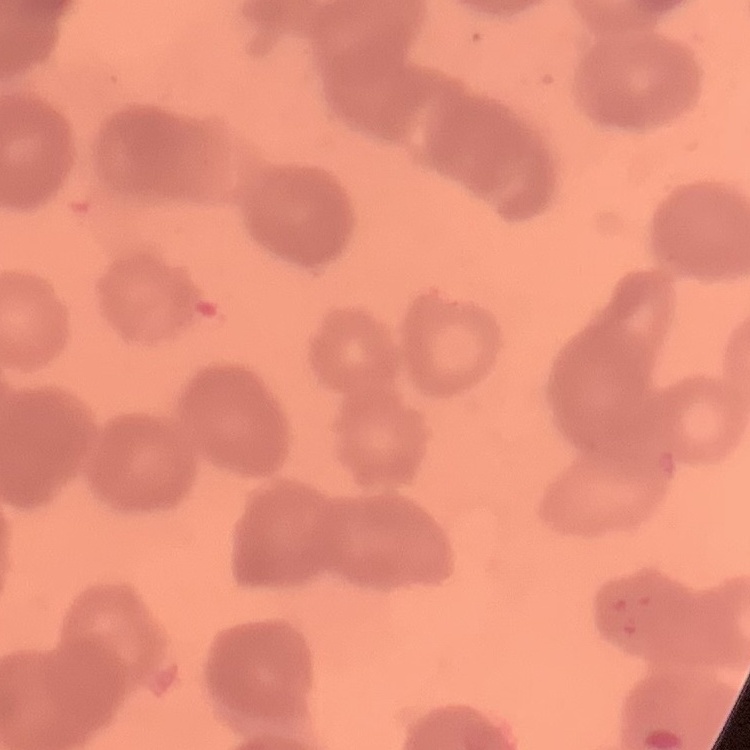

Summary:
  - Erythrocyte morphology: rouleaux formation
  - Stain: Field's or Giemsa
  - Image type: one tile cut from a larger photomicrograph
  - Preparation: thin blood smear